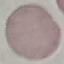
{
  "malaria_status": "uninfected",
  "image_type": "cell patch, automatically extracted from a larger field of view and resized to 64 × 64 pixels",
  "preparation": "thin blood film",
  "capture": "smartphone camera at the microscope eyepiece",
  "stain": "Giemsa"
}